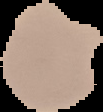
preparation = thin blood smear
image size = 103×112 pixels
image type = segmented cell region with the area outside set to black
result = malaria parasites detected